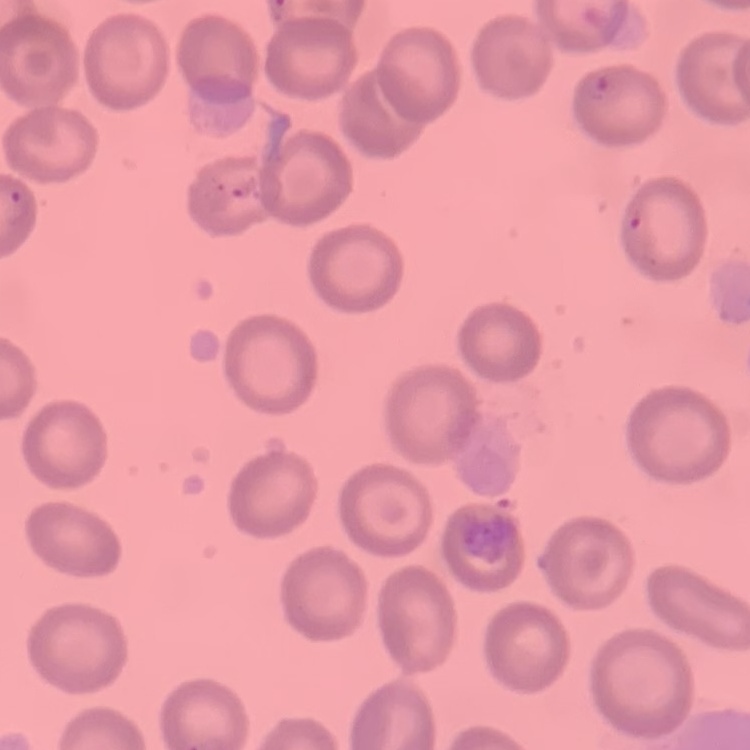

Summary:
  - Erythrocyte morphology: no rouleaux formation
  - Preparation: thin blood film
  - Image type: square crop of a larger photomicrograph
  - Stain: Field's or Giemsa